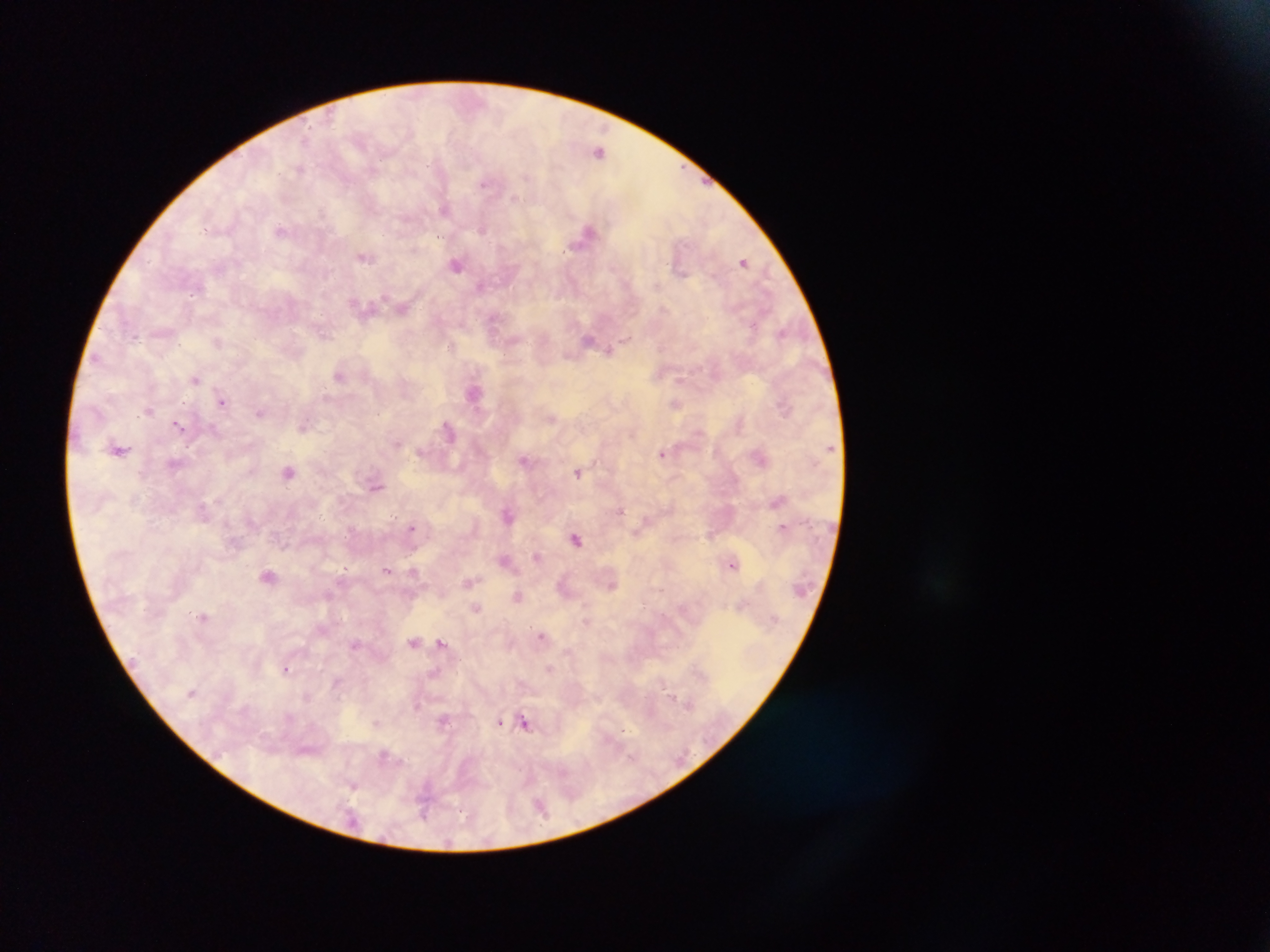

Approximate centers as (x, y) in pixels. Plasmodium parasite locations: (599, 152), (301, 169), (485, 183), (515, 198), (444, 210), (483, 229), (280, 230), (587, 232), (365, 257), (743, 261), (456, 265), (657, 285), (479, 286), (197, 288), (403, 307), (782, 333), (325, 334), (589, 339), (626, 339), (452, 344), (609, 351), (339, 376), (195, 379), (680, 380), (473, 394), (223, 402), (675, 404), (149, 410), (260, 412), (552, 417), (178, 425), (303, 426), (215, 429), (449, 430), (397, 443), (119, 449), (662, 453), (524, 460), (289, 472), (578, 473), (377, 487), (621, 510), (507, 515), (411, 527), (782, 527), (577, 539), (537, 556), (505, 560), (732, 565), (344, 568), (387, 570), (413, 571), (269, 576), (468, 582), (612, 586), (518, 596), (476, 607), (204, 616), (586, 621), (541, 636), (414, 642), (442, 643), (355, 644), (549, 668), (286, 669), (669, 691), (192, 693), (688, 703), (444, 719), (499, 721), (376, 723), (525, 723), (624, 730), (384, 756), (354, 785), (425, 801), (540, 805). Collected in Ghana. Thick blood film. Image is 1270×952 pixels. Single field of view. Mobile-phone photograph taken through the microscope.